Assess the morphology of the erythrocytes.
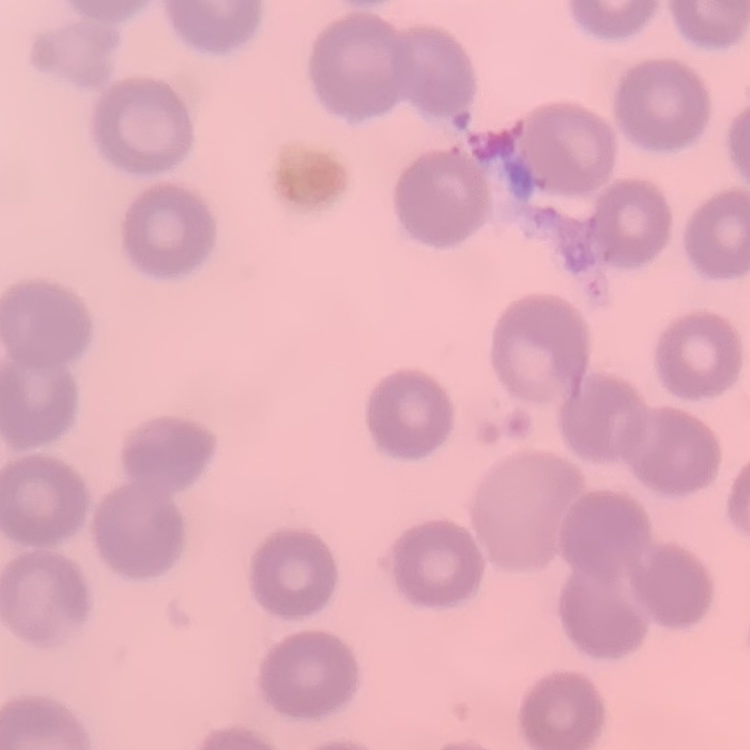
No rouleaux formation.

preparation = thin peripheral smear
stain = Field's or Giemsa
image type = square crop of a larger photomicrograph